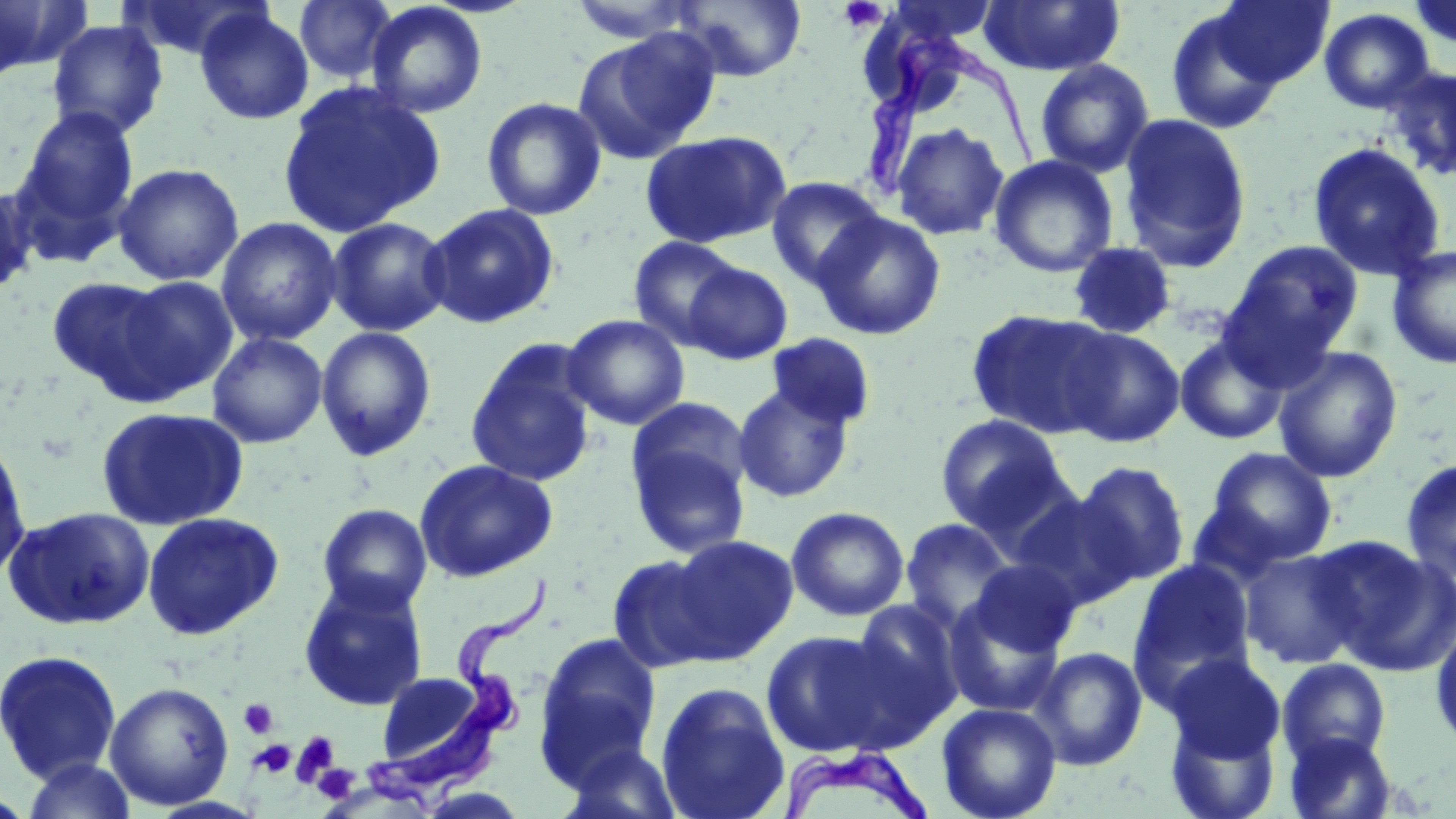
Summary:
  - Coordinate format: approximate bounding boxes as named x1/y1/x2/y2 corners in pixels
  - Trypanosoma brucei locations: (x1=860, y1=30, x2=1042, y2=207), (x1=366, y1=577, x2=559, y2=809), (x1=780, y1=743, x2=933, y2=819)
  - Uninfected red blood cell locations: (x1=0, y1=0, x2=89, y2=79), (x1=120, y1=0, x2=267, y2=62), (x1=293, y1=0, x2=398, y2=84), (x1=566, y1=0, x2=706, y2=43), (x1=671, y1=0, x2=807, y2=82), (x1=887, y1=0, x2=1001, y2=47), (x1=978, y1=0, x2=1124, y2=77), (x1=1213, y1=1, x2=1334, y2=89), (x1=365, y1=2, x2=488, y2=118), (x1=194, y1=6, x2=314, y2=125), (x1=1165, y1=7, x2=1285, y2=135), (x1=1318, y1=8, x2=1435, y2=113), (x1=46, y1=19, x2=169, y2=140), (x1=574, y1=29, x2=721, y2=163), (x1=1035, y1=59, x2=1155, y2=178), (x1=1384, y1=67, x2=1456, y2=180), (x1=277, y1=80, x2=445, y2=237), (x1=482, y1=97, x2=606, y2=220), (x1=13, y1=105, x2=140, y2=251), (x1=1118, y1=112, x2=1252, y2=273), (x1=890, y1=122, x2=1009, y2=241), (x1=640, y1=129, x2=792, y2=249), (x1=1308, y1=142, x2=1445, y2=280), (x1=989, y1=154, x2=1119, y2=278), (x1=112, y1=162, x2=244, y2=286), (x1=766, y1=176, x2=886, y2=289), (x1=0, y1=182, x2=38, y2=296), (x1=421, y1=202, x2=560, y2=330), (x1=812, y1=211, x2=947, y2=340), (x1=326, y1=216, x2=452, y2=337), (x1=216, y1=217, x2=342, y2=346), (x1=628, y1=235, x2=742, y2=349), (x1=1221, y1=240, x2=1363, y2=371), (x1=1067, y1=242, x2=1178, y2=340), (x1=1386, y1=245, x2=1456, y2=369), (x1=682, y1=262, x2=793, y2=364), (x1=46, y1=275, x2=175, y2=396), (x1=111, y1=275, x2=240, y2=401), (x1=966, y1=308, x2=1117, y2=438), (x1=562, y1=314, x2=690, y2=430), (x1=315, y1=326, x2=437, y2=461), (x1=1060, y1=326, x2=1185, y2=447), (x1=207, y1=332, x2=328, y2=448), (x1=765, y1=332, x2=877, y2=432), (x1=1174, y1=334, x2=1290, y2=445), (x1=465, y1=339, x2=598, y2=487), (x1=1272, y1=346, x2=1403, y2=483), (x1=732, y1=383, x2=854, y2=503), (x1=96, y1=406, x2=249, y2=531), (x1=935, y1=414, x2=1069, y2=534), (x1=627, y1=426, x2=752, y2=559), (x1=0, y1=436, x2=32, y2=586), (x1=1204, y1=446, x2=1338, y2=565), (x1=1400, y1=458, x2=1456, y2=583), (x1=413, y1=459, x2=558, y2=581), (x1=1074, y1=459, x2=1191, y2=586), (x1=1009, y1=492, x2=1139, y2=609), (x1=317, y1=503, x2=433, y2=615), (x1=4, y1=506, x2=155, y2=631), (x1=787, y1=506, x2=909, y2=621), (x1=142, y1=512, x2=284, y2=640), (x1=899, y1=518, x2=1017, y2=633), (x1=663, y1=534, x2=799, y2=662), (x1=1319, y1=537, x2=1456, y2=675), (x1=1239, y1=548, x2=1362, y2=669), (x1=606, y1=554, x2=727, y2=672), (x1=1129, y1=558, x2=1256, y2=697), (x1=969, y1=559, x2=1082, y2=656), (x1=298, y1=578, x2=429, y2=711), (x1=943, y1=596, x2=1067, y2=716), (x1=849, y1=600, x2=964, y2=729), (x1=1431, y1=621, x2=1456, y2=752), (x1=761, y1=629, x2=909, y2=757), (x1=534, y1=631, x2=662, y2=777), (x1=1029, y1=646, x2=1147, y2=771), (x1=0, y1=649, x2=122, y2=784), (x1=1165, y1=654, x2=1285, y2=764), (x1=1277, y1=658, x2=1391, y2=767), (x1=374, y1=671, x2=491, y2=771), (x1=104, y1=682, x2=234, y2=810), (x1=655, y1=682, x2=790, y2=819), (x1=936, y1=702, x2=1061, y2=819), (x1=1165, y1=711, x2=1281, y2=819), (x1=1284, y1=731, x2=1397, y2=819), (x1=559, y1=740, x2=685, y2=819), (x1=20, y1=757, x2=138, y2=819)
  - Platelet locations: (x1=836, y1=3, x2=888, y2=32), (x1=238, y1=698, x2=279, y2=739), (x1=291, y1=730, x2=340, y2=786), (x1=251, y1=739, x2=296, y2=778), (x1=312, y1=764, x2=360, y2=804)
  - Slide-level diagnosis: Trypanosoma brucei
  - Stain: May-Grünwald-Giemsa
  - Preparation: thin blood film
  - Field of view: single
  - Magnification: 1000x
  - Image size: 1456×819 pixels
  - Modality: light microscopy